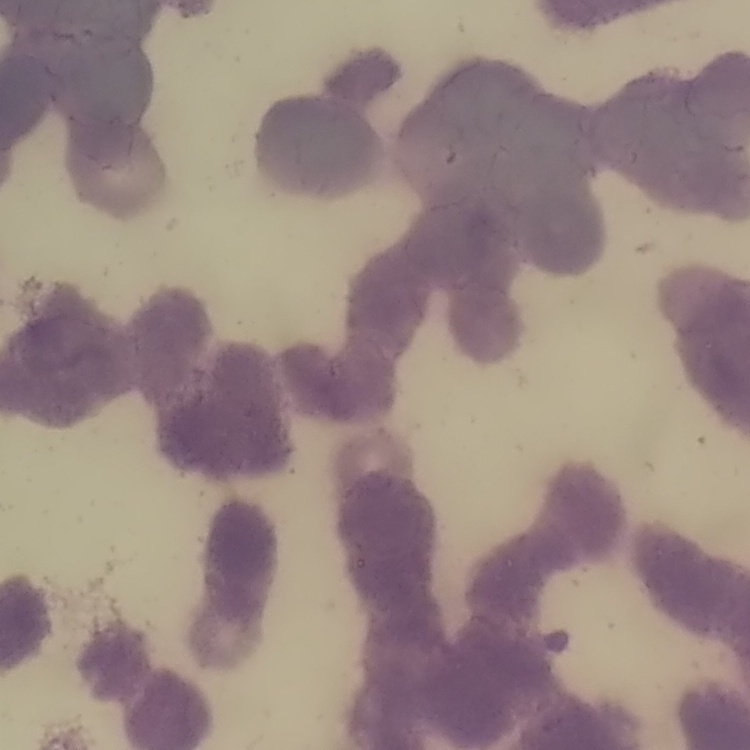
Summary:
  - Erythrocyte morphology: rouleaux formation
  - Image type: one tile cut from a larger photomicrograph
  - Preparation: thin blood smear
  - Stain: Field's or Giemsa